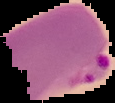

Summary:
  - Image size: 115×103 pixels
  - Result: malaria parasites identified
  - Image type: cell region segmented out of the field of view; surrounding area masked to black
  - Preparation: thin blood film